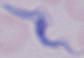

Micrograph. A trypanosome is shown. Captured at 1000x magnification.